Assess the morphology of the red blood cells.
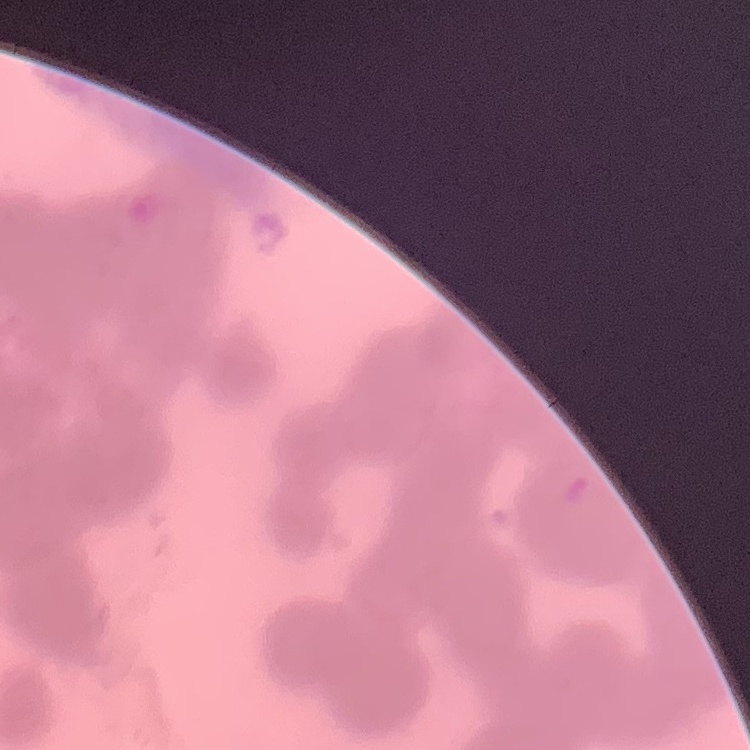

Rouleaux formation.

Summary:
  - Preparation: thin blood smear
  - Stain: Field's or Giemsa
  - Image type: square crop of a larger photomicrograph